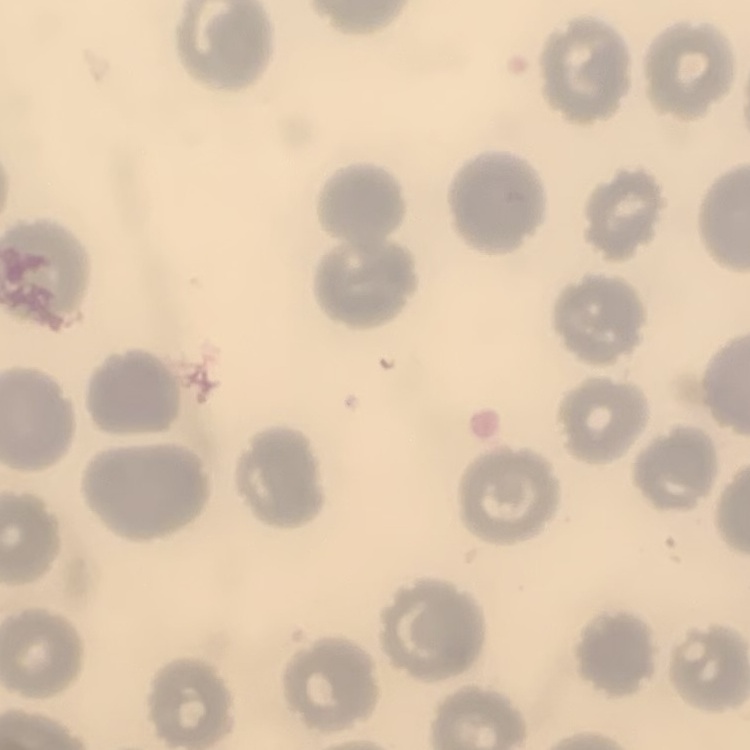
The erythrocytes exhibit no rouleaux formation. Square crop of a larger photomicrograph. Thin blood smear. Stained with either Field's or Giemsa.